Report the malaria status of this cell.
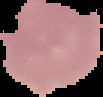

Uninfected.

Summary:
  - Image size: 103×97 pixels
  - Image type: segmented cell region with the area outside set to black
  - Preparation: thin blood film